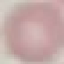

result = negative for malaria parasites
stain = Giemsa
image type = automatically extracted cell patch, resized to 64 × 64 pixels
preparation = thin smear
capture = smartphone camera at the microscope eyepiece